Look for Plasmodium parasites.
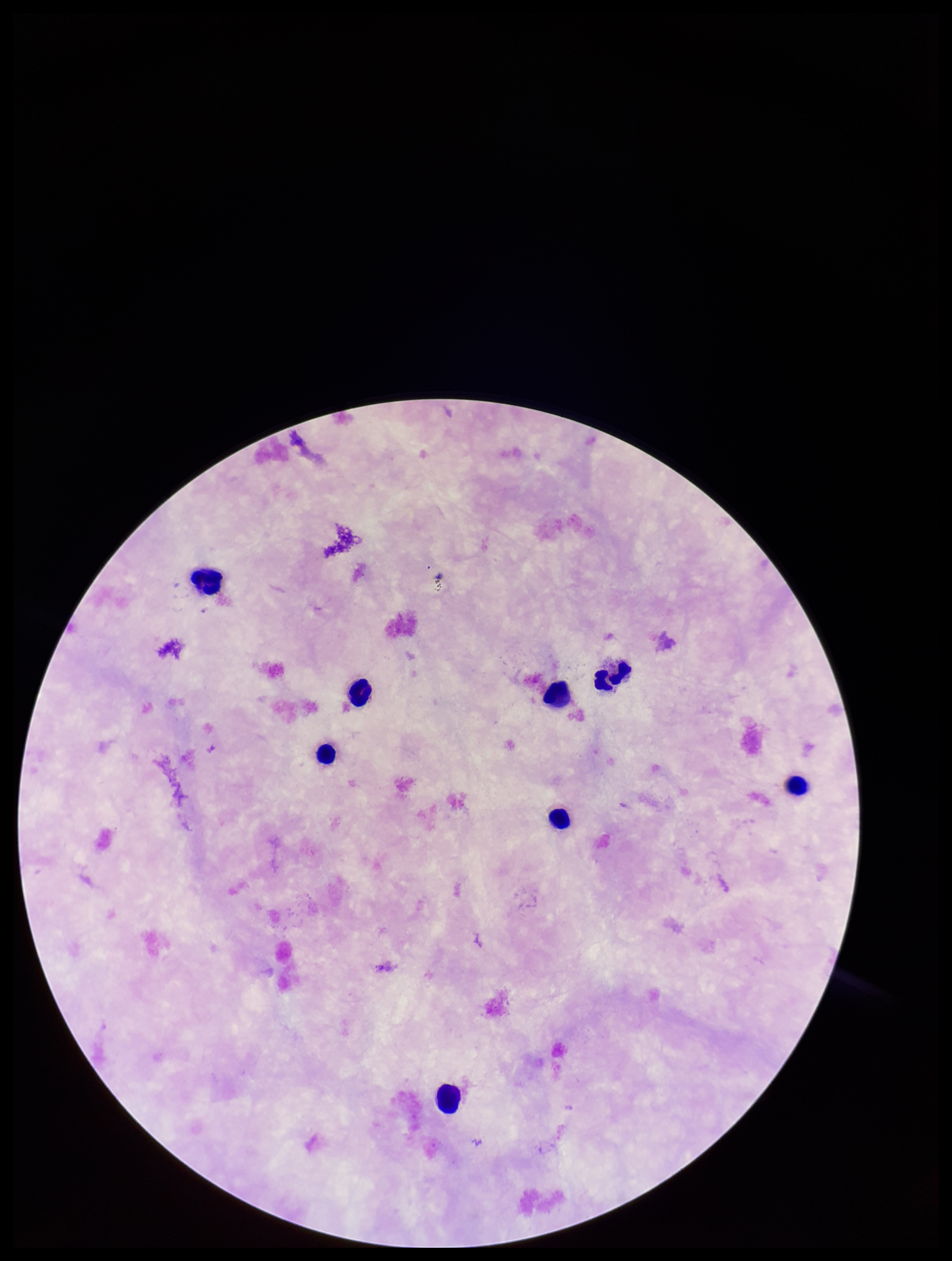
None detected.

{
  "capture": "smartphone photograph through the microscope eyepiece",
  "patient_malaria_status": "negative",
  "field_of_view": "single",
  "image_size": "952×1261 pixels",
  "stain": "Giemsa",
  "parasite_count": 0,
  "leukocyte_count": 8,
  "preparation": "thick blood smear"
}